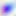

Summary:
  - Modality: photomicrograph
  - Identification: Toxoplasma gondii
  - Magnification: 400x